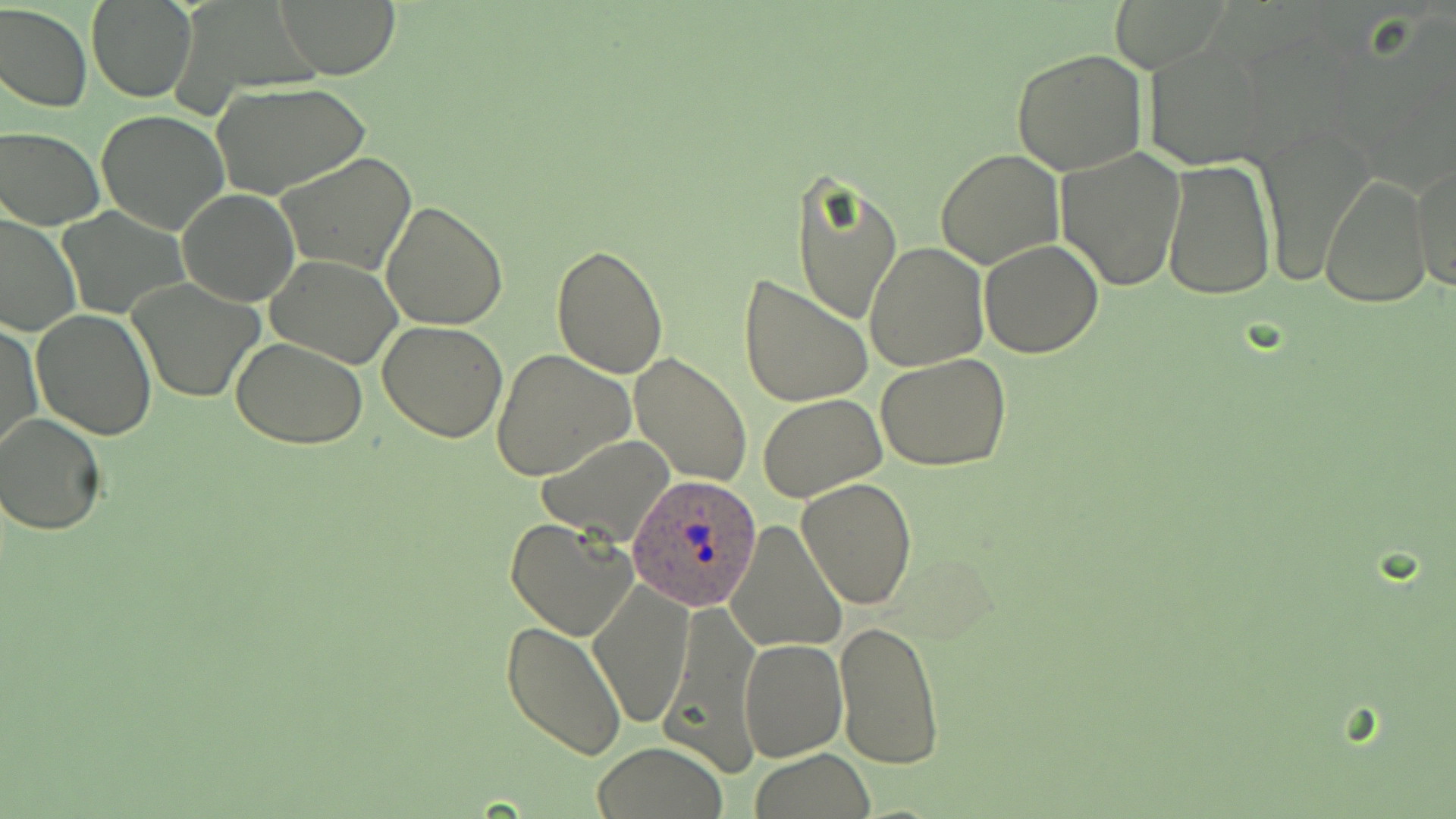

slide-level diagnosis = Plasmodium ovale
preparation = thin blood film
uninfected red blood cell locations = approximate bounding boxes as [x1, y1, x2, y2] in pixels: [86, 0, 196, 102], [276, 1, 400, 80], [0, 3, 92, 113], [1143, 41, 1275, 168], [1011, 48, 1147, 174], [210, 81, 372, 200], [96, 110, 231, 235], [1256, 119, 1378, 285], [1, 125, 105, 229], [1055, 147, 1186, 291], [935, 148, 1065, 270], [277, 151, 418, 277], [1411, 153, 1455, 293], [1161, 160, 1276, 301], [790, 169, 903, 327], [1319, 173, 1432, 307], [177, 189, 299, 307], [381, 202, 508, 332], [58, 207, 189, 321], [1, 213, 78, 337], [864, 240, 988, 371], [978, 240, 1104, 358], [550, 244, 669, 379], [267, 255, 403, 368], [737, 274, 873, 408], [128, 280, 264, 402], [32, 310, 156, 439], [378, 321, 509, 441], [1, 322, 42, 457], [231, 339, 370, 450], [490, 349, 635, 481], [628, 352, 752, 487], [876, 354, 1012, 471], [758, 394, 887, 501], [1, 414, 106, 534], [538, 436, 674, 545], [796, 477, 919, 610], [505, 518, 638, 639], [725, 521, 847, 653], [588, 581, 694, 728], [660, 600, 760, 780], [834, 618, 944, 771], [502, 620, 629, 761], [740, 638, 847, 762], [591, 743, 727, 818], [749, 749, 876, 819]
field of view = single
image size = 1456×819 pixels
magnification = 1000x
Plasmodium ovale-infected red blood cell locations = approximate bounding boxes as [x1, y1, x2, y2] in pixels: [627, 472, 762, 609]
stain = May-Grünwald-Giemsa
modality = light microscopy